State the blood parasite species.
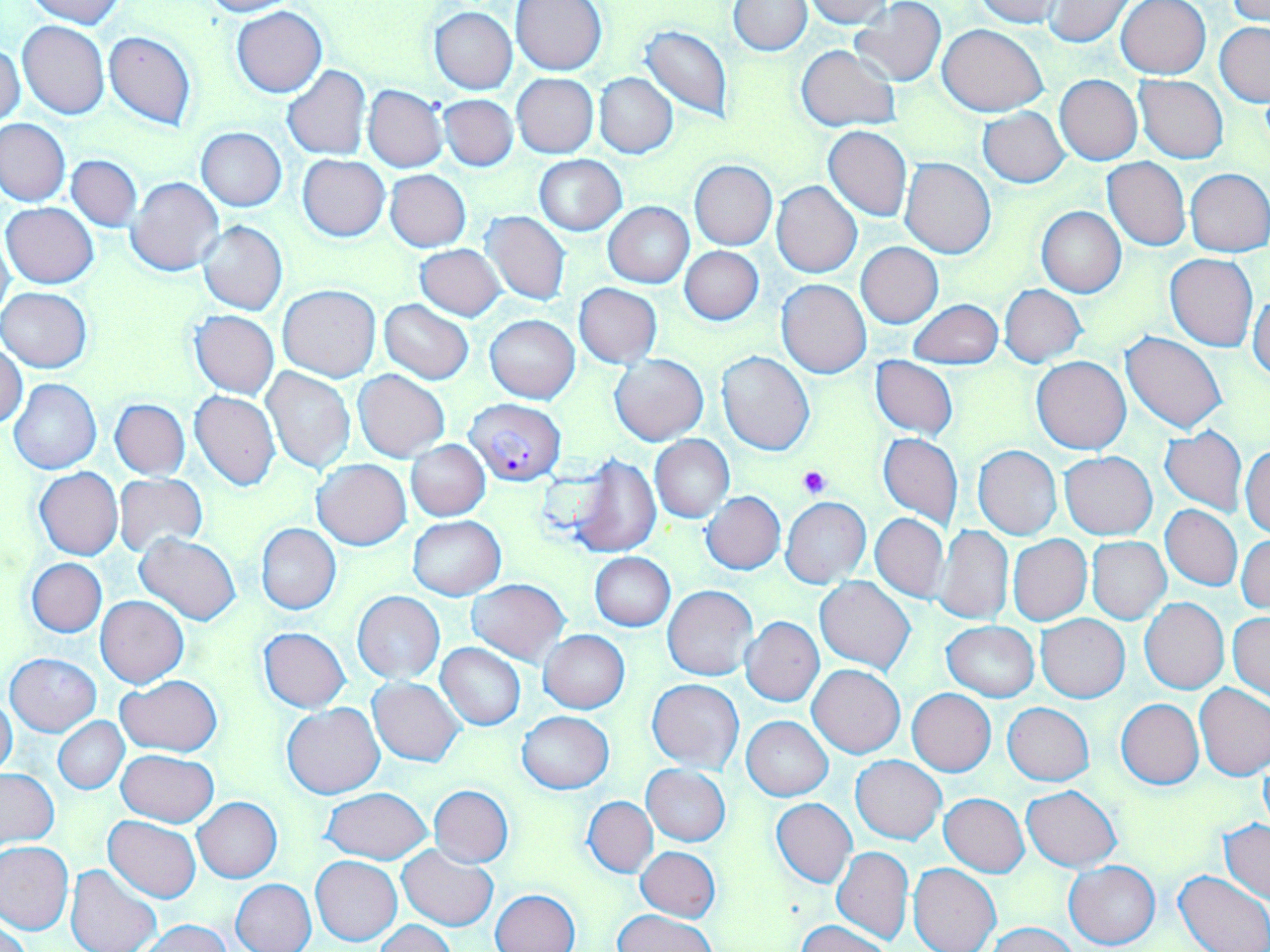
Plasmodium falciparum.

Approximate bounding boxes as [x1, y1, x2, y2] in pixels. Platelet locations: [798, 464, 832, 499]. Plasmodium falciparum-infected red blood cell locations: [466, 399, 566, 485]. Uninfected red blood cell locations: [22, 0, 124, 27], [198, 0, 297, 16], [803, 0, 895, 27], [973, 0, 1066, 27], [1225, 0, 1270, 24], [511, 1, 608, 75], [730, 1, 811, 55], [1043, 1, 1133, 47], [1115, 1, 1211, 79], [849, 2, 947, 86], [232, 6, 329, 98], [429, 7, 517, 94], [18, 21, 109, 119], [1215, 22, 1270, 106], [640, 23, 734, 124], [937, 23, 1048, 116], [104, 31, 196, 131], [0, 43, 25, 128], [795, 45, 901, 132], [281, 66, 371, 160], [512, 73, 599, 158], [594, 73, 679, 158], [1055, 75, 1143, 166], [1135, 75, 1227, 163], [363, 85, 449, 173], [439, 94, 518, 170], [978, 108, 1070, 187], [0, 118, 70, 207], [823, 126, 912, 222], [196, 128, 287, 211], [298, 154, 390, 241], [533, 154, 626, 236], [67, 155, 142, 231], [1103, 157, 1191, 251], [899, 158, 997, 260], [690, 159, 777, 248], [1185, 168, 1269, 256], [385, 171, 471, 251], [127, 177, 224, 277], [772, 181, 861, 278], [603, 202, 694, 288], [3, 203, 99, 288], [1037, 205, 1126, 297], [481, 211, 571, 306], [198, 220, 287, 315], [0, 231, 14, 326], [857, 243, 943, 327], [415, 244, 506, 319], [680, 246, 764, 324], [1165, 254, 1257, 351], [776, 280, 872, 378], [573, 283, 663, 367], [999, 284, 1086, 366], [277, 285, 380, 381], [0, 288, 93, 372], [1249, 291, 1270, 380], [378, 299, 474, 384], [909, 299, 1003, 370], [189, 310, 279, 399], [485, 314, 579, 403], [1122, 333, 1227, 433], [1, 341, 26, 431], [717, 351, 815, 455], [610, 354, 709, 445], [870, 356, 957, 440], [1032, 357, 1131, 454], [261, 367, 354, 473], [354, 369, 449, 462], [9, 378, 102, 475], [189, 390, 280, 490], [110, 399, 190, 479], [1159, 426, 1247, 518], [878, 432, 962, 530], [650, 435, 734, 523], [406, 440, 490, 520], [1242, 442, 1270, 537], [973, 445, 1062, 540], [1059, 452, 1158, 539], [567, 453, 661, 558], [312, 459, 411, 549], [34, 467, 123, 560], [114, 473, 208, 559], [701, 492, 785, 575], [782, 497, 870, 587], [1161, 505, 1242, 590], [870, 513, 948, 603], [407, 516, 505, 600], [255, 523, 341, 614], [937, 526, 1013, 625], [134, 533, 241, 625], [1236, 534, 1270, 616], [1008, 535, 1092, 626], [1087, 537, 1171, 624], [589, 553, 675, 631], [27, 558, 106, 637], [815, 576, 915, 673], [468, 579, 570, 663], [663, 586, 757, 679], [352, 591, 445, 682], [95, 595, 190, 687], [1140, 598, 1229, 694], [1228, 611, 1269, 702], [1036, 615, 1129, 702], [741, 617, 824, 707], [942, 621, 1038, 701], [258, 627, 351, 711], [539, 630, 630, 713], [437, 643, 525, 730], [5, 652, 101, 736], [808, 664, 905, 758], [115, 676, 223, 756], [369, 677, 464, 766], [646, 679, 744, 771], [1195, 684, 1270, 781], [907, 688, 996, 777], [0, 698, 18, 777], [1116, 698, 1203, 790], [1004, 702, 1094, 785], [282, 703, 386, 799], [516, 711, 615, 794], [53, 716, 129, 794], [742, 716, 832, 800], [116, 749, 218, 827], [850, 754, 945, 843], [642, 765, 730, 846], [0, 768, 60, 850], [429, 785, 514, 867], [1022, 786, 1121, 871], [320, 788, 433, 863], [940, 793, 1030, 876], [193, 797, 282, 883], [584, 797, 658, 877], [770, 798, 855, 887], [104, 817, 202, 902], [1221, 818, 1269, 904], [0, 841, 73, 935], [398, 846, 498, 930], [831, 846, 912, 944], [636, 847, 720, 922], [311, 855, 402, 946], [1064, 861, 1160, 949], [908, 863, 1000, 952], [67, 865, 162, 952], [1173, 871, 1270, 952], [232, 878, 317, 952], [489, 889, 580, 952], [614, 910, 716, 952], [139, 918, 233, 951], [798, 919, 889, 952], [374, 921, 454, 952], [986, 922, 1078, 952]. Image is 1270×952 pixels. Light microscopy. May-Grünwald-Giemsa-stained preparation. 1000x magnification. Thin blood film. One field of a larger specimen.